Describe the morphology of the red blood cells.
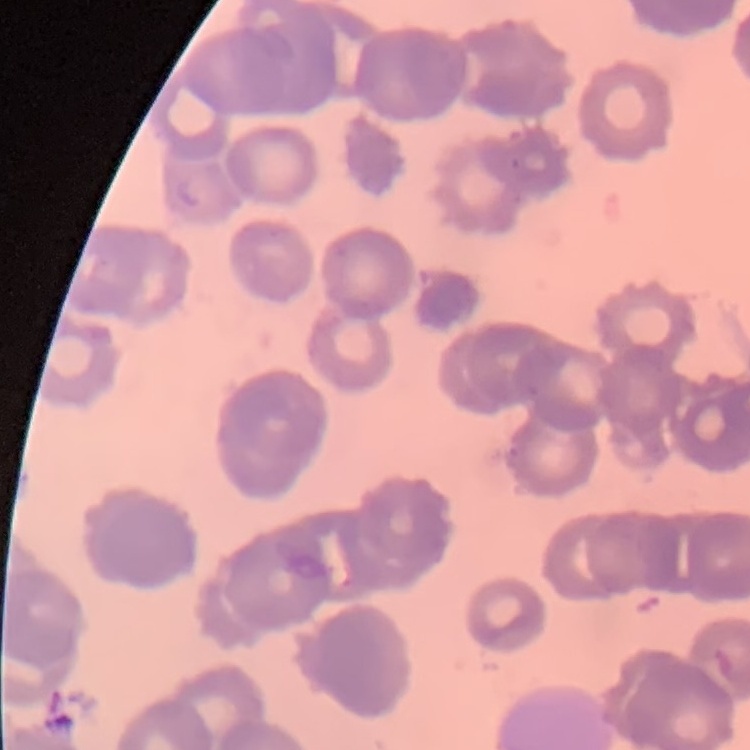

Rouleaux formation.

preparation = thin blood film
stain = Field's or Giemsa
image type = one tile cut from a larger photomicrograph